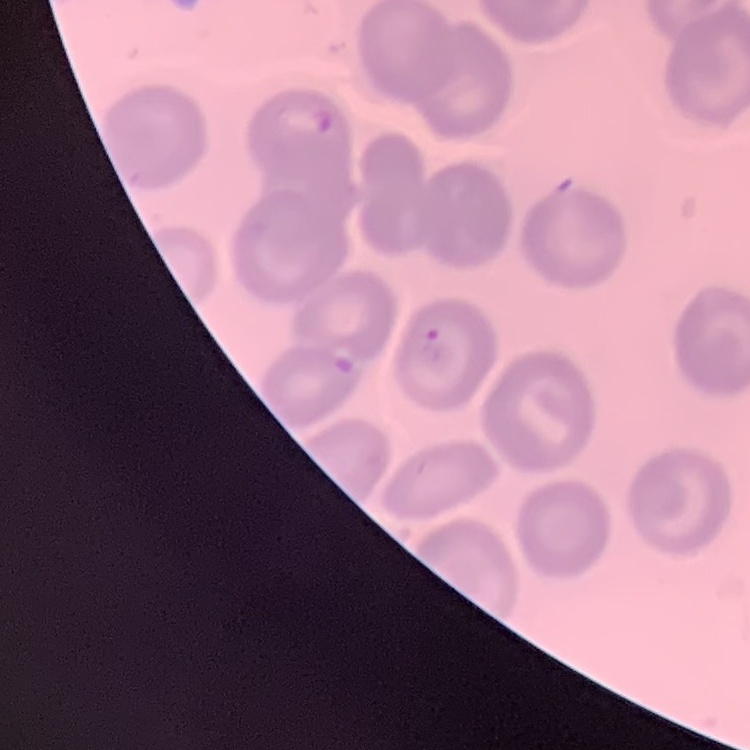

The red blood cells exhibit no rouleaux formation. One tile cut from a larger photomicrograph. Field's or Giemsa stain. Thin peripheral smear.